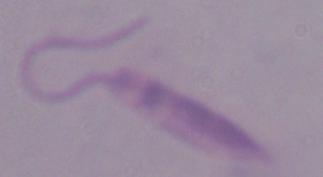

A Leishmania parasite is seen. Captured at 1000x magnification. Micrograph.